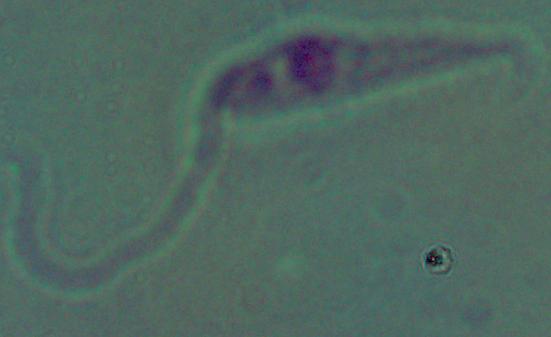

{
  "identification": "Leishmania",
  "modality": "micrograph",
  "magnification": "1000x"
}